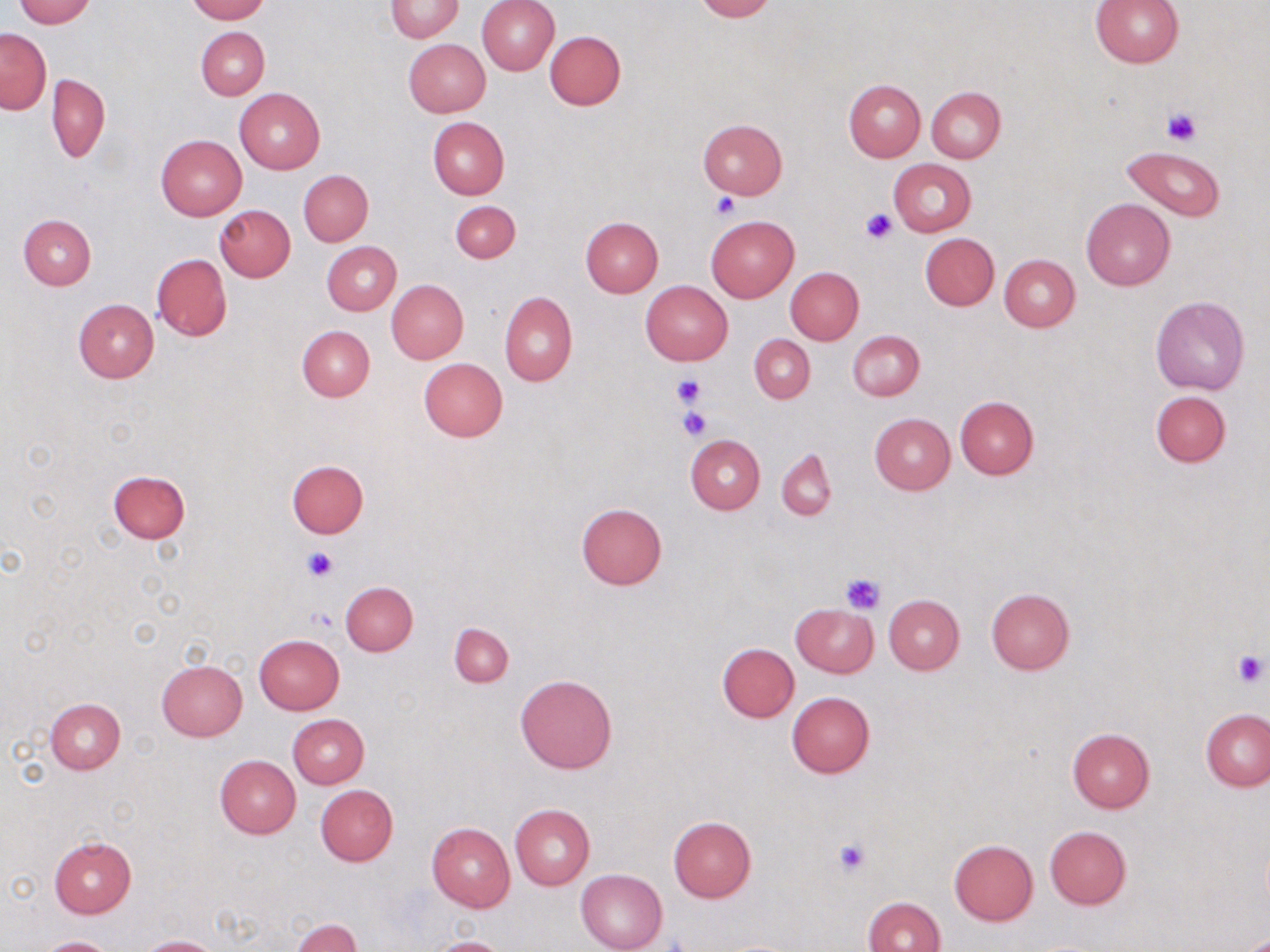

slide-level diagnosis = negative for blood parasites
field of view = single
uninfected red blood cell locations = approximate bounding boxes as (x1, y1, x2, y2) in pixels: (12, 0, 96, 26), (185, 0, 268, 23), (477, 0, 559, 75), (694, 0, 776, 22), (385, 1, 464, 41), (1090, 1, 1184, 66), (196, 26, 269, 99), (0, 28, 51, 113), (544, 30, 625, 111), (404, 39, 490, 117), (46, 73, 110, 163), (844, 80, 925, 161), (926, 85, 1005, 162), (234, 87, 326, 174), (428, 116, 509, 200), (696, 119, 788, 198), (156, 134, 246, 220), (1121, 147, 1223, 220), (889, 159, 976, 236), (299, 170, 373, 246), (1081, 198, 1176, 290), (449, 201, 521, 263), (214, 206, 296, 281), (19, 213, 95, 289), (705, 214, 798, 301), (581, 217, 663, 296), (921, 233, 999, 311), (322, 241, 401, 315), (152, 253, 232, 340), (998, 253, 1081, 332), (785, 268, 864, 344), (387, 279, 468, 364), (640, 280, 732, 365), (498, 291, 577, 386), (1151, 296, 1250, 395), (73, 299, 158, 383), (298, 325, 376, 401), (847, 330, 924, 401), (749, 335, 814, 403), (418, 358, 507, 442), (1150, 390, 1231, 467), (955, 397, 1038, 479), (869, 412, 955, 495), (685, 434, 765, 513), (777, 448, 837, 522), (286, 459, 369, 538), (107, 470, 190, 542), (575, 503, 668, 590), (340, 581, 417, 656), (985, 588, 1074, 675), (884, 594, 965, 674), (791, 603, 878, 677), (449, 623, 513, 687), (253, 634, 344, 715), (717, 643, 799, 723), (156, 659, 247, 740), (515, 675, 618, 774), (786, 691, 874, 779), (45, 697, 125, 774), (1200, 709, 1270, 792), (288, 714, 369, 788), (1067, 729, 1155, 813), (214, 755, 300, 839), (315, 784, 398, 867), (510, 804, 594, 889), (669, 816, 756, 901), (427, 822, 515, 912), (1044, 825, 1132, 909), (49, 838, 136, 918), (948, 839, 1038, 925), (576, 869, 668, 952), (862, 896, 946, 952), (290, 917, 362, 952), (137, 936, 223, 952), (426, 936, 510, 952), (35, 937, 122, 952)
modality = optical microscopy
platelet locations = approximate bounding boxes as (x1, y1, x2, y2) in pixels: (1163, 107, 1199, 146), (712, 194, 740, 219), (861, 208, 896, 243), (671, 374, 705, 409), (679, 406, 713, 440), (302, 548, 336, 583), (841, 572, 886, 614), (303, 607, 337, 634), (1232, 651, 1268, 686), (835, 838, 869, 875)
image size = 1270×952 pixels
stain = May-Grünwald-Giemsa
preparation = thin blood film
magnification = 1000x